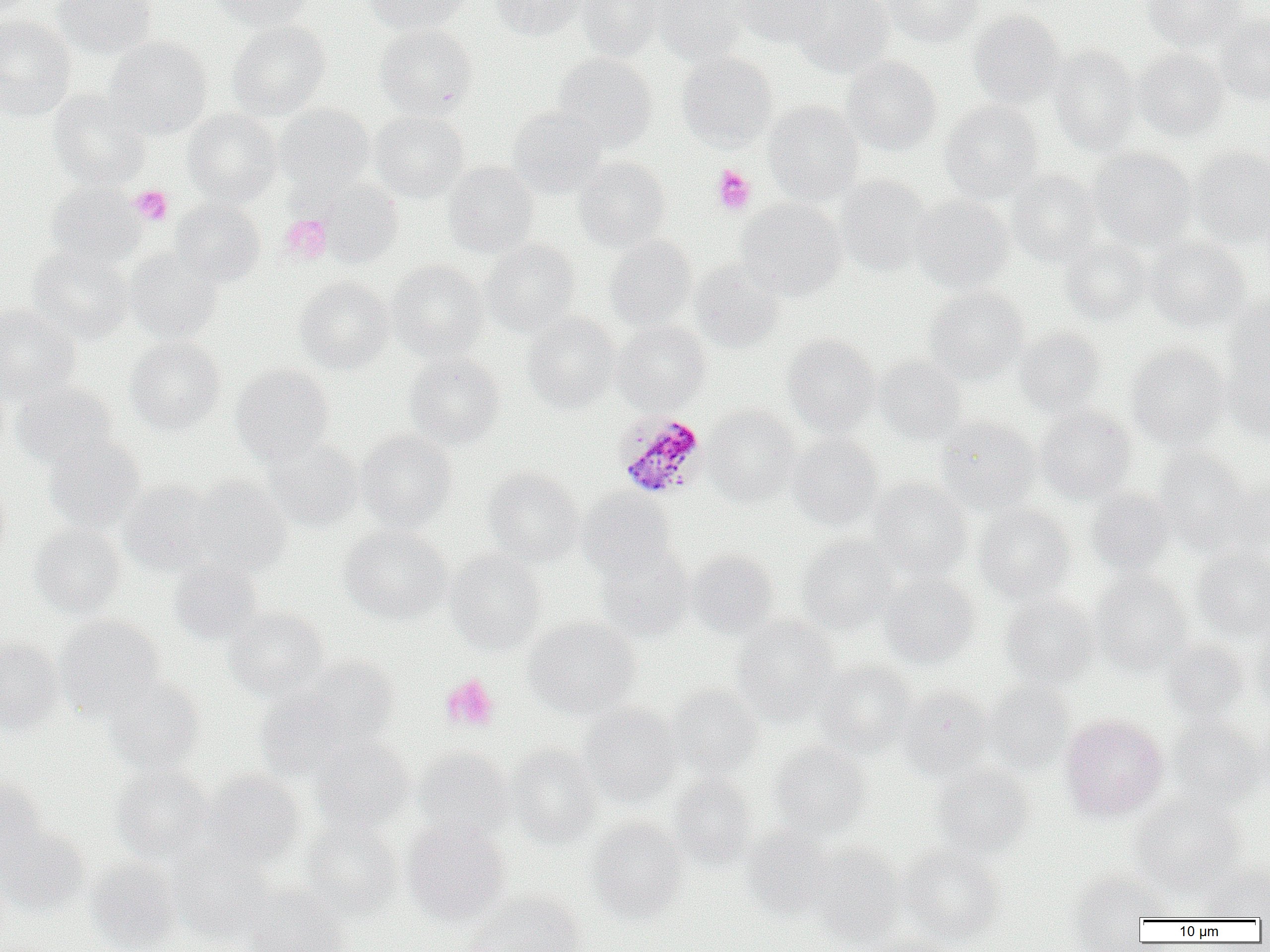 Approximate bounding boxes as [x1, y1, x2, y2] in pixels. Plasmodium malariae-infected red blood cell locations: [613, 411, 708, 500]. Uninfected red blood cell locations: [52, 0, 158, 58], [208, 0, 312, 30], [363, 0, 472, 35], [490, 0, 585, 41], [576, 0, 665, 60], [652, 0, 749, 66], [732, 0, 828, 48], [789, 0, 894, 77], [881, 0, 983, 47], [1141, 0, 1247, 49], [969, 11, 1066, 106], [0, 15, 75, 120], [1216, 15, 1270, 107], [227, 20, 332, 119], [375, 23, 478, 118], [104, 37, 212, 140], [1048, 45, 1142, 155], [1133, 48, 1229, 141], [676, 52, 778, 153], [554, 53, 657, 151], [841, 55, 942, 155], [47, 90, 150, 191], [940, 100, 1045, 202], [764, 101, 864, 204], [276, 104, 375, 196], [508, 108, 606, 198], [182, 109, 283, 206], [370, 111, 469, 202], [1190, 146, 1270, 247], [1088, 148, 1196, 251], [573, 156, 670, 251], [443, 161, 539, 258], [1006, 170, 1103, 265], [835, 175, 932, 274], [318, 179, 402, 267], [45, 182, 145, 270], [909, 195, 1014, 293], [170, 198, 265, 286], [736, 199, 846, 300], [604, 235, 697, 330], [1146, 236, 1250, 333], [1059, 238, 1153, 325], [482, 239, 579, 337], [28, 246, 134, 344], [124, 249, 222, 344], [386, 260, 489, 360], [689, 261, 786, 352], [295, 277, 393, 373], [925, 286, 1028, 384], [1227, 294, 1270, 384], [0, 304, 81, 405], [523, 312, 620, 412], [612, 321, 711, 413], [1015, 328, 1107, 419], [783, 334, 880, 436], [125, 336, 225, 434], [1127, 344, 1228, 448], [404, 353, 505, 450], [1222, 354, 1270, 442], [874, 356, 966, 444], [230, 363, 334, 462], [0, 378, 10, 461], [12, 382, 117, 468], [703, 405, 801, 506], [1035, 407, 1137, 503], [935, 417, 1041, 512], [355, 430, 456, 532], [787, 432, 882, 529], [43, 437, 146, 531], [262, 437, 363, 531], [1153, 449, 1254, 550], [483, 467, 584, 566], [188, 476, 292, 574], [1223, 477, 1270, 553], [868, 479, 971, 580], [120, 480, 221, 575], [0, 482, 10, 573], [1085, 488, 1175, 575], [579, 489, 676, 575], [974, 503, 1076, 603], [30, 523, 125, 618], [340, 525, 452, 624], [796, 536, 899, 633], [597, 546, 693, 640], [1192, 546, 1270, 639], [445, 550, 547, 653], [686, 551, 777, 638], [168, 558, 264, 647], [879, 572, 980, 667], [1091, 572, 1193, 675], [1000, 592, 1098, 688], [224, 606, 328, 701], [56, 616, 165, 719], [731, 616, 839, 723], [524, 617, 640, 718], [1254, 622, 1270, 714], [0, 638, 63, 735], [1162, 639, 1250, 724], [300, 656, 400, 747], [815, 660, 916, 757], [103, 675, 204, 773], [980, 680, 1074, 776], [666, 685, 763, 779], [897, 687, 991, 778], [256, 689, 358, 782], [578, 704, 683, 805], [1253, 711, 1270, 800], [1060, 713, 1169, 821], [1168, 716, 1265, 809], [311, 736, 414, 833], [768, 741, 871, 838], [506, 745, 602, 848], [413, 746, 514, 842], [931, 763, 1034, 858], [111, 764, 216, 864], [200, 770, 306, 866], [669, 773, 758, 870], [0, 775, 46, 868], [1130, 793, 1248, 895], [300, 817, 402, 917], [402, 818, 511, 924], [587, 818, 688, 921], [0, 824, 90, 915], [742, 826, 833, 919], [808, 844, 905, 946], [169, 845, 276, 944], [899, 846, 1004, 944], [85, 857, 181, 952], [1198, 862, 1270, 921], [1067, 870, 1168, 948], [243, 884, 350, 952], [465, 891, 585, 952], [866, 932, 961, 952]. Platelet locations: [712, 165, 756, 215], [129, 185, 173, 226], [279, 214, 332, 264], [440, 674, 500, 733]. Slide-level diagnosis: Plasmodium malariae. Single field of view. Image is 1270×952 pixels. 1000x magnification. Thin blood smear. Optical microscopy.